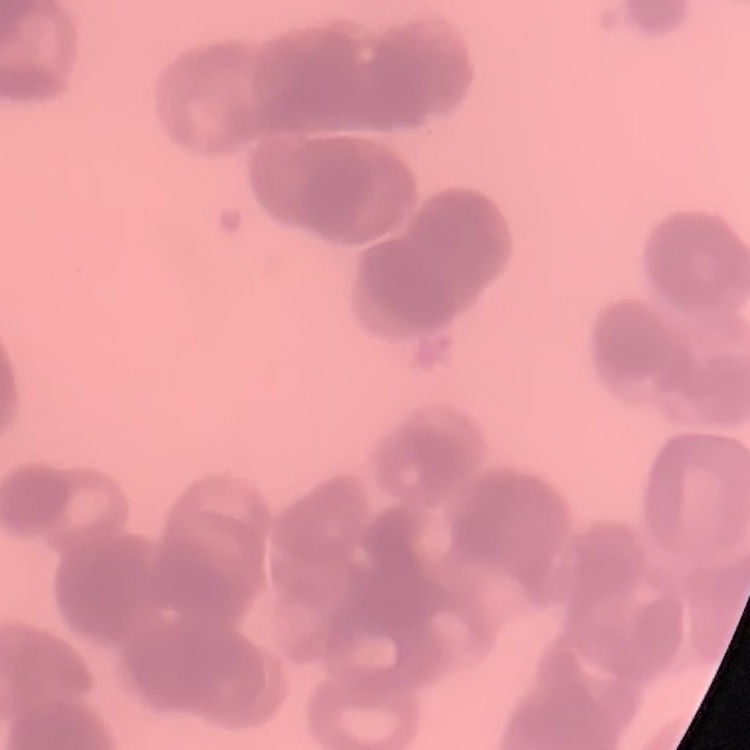 The erythrocytes show rouleaux formation. Thin blood film. Stained with either Field's or Giemsa. One tile cut from a larger photomicrograph.